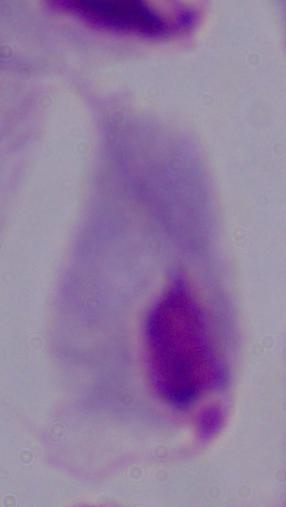
magnification = 1000x
modality = photomicrograph
identification = trichomonad